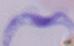

identification = trypanosome
modality = photomicrograph
magnification = 1000x